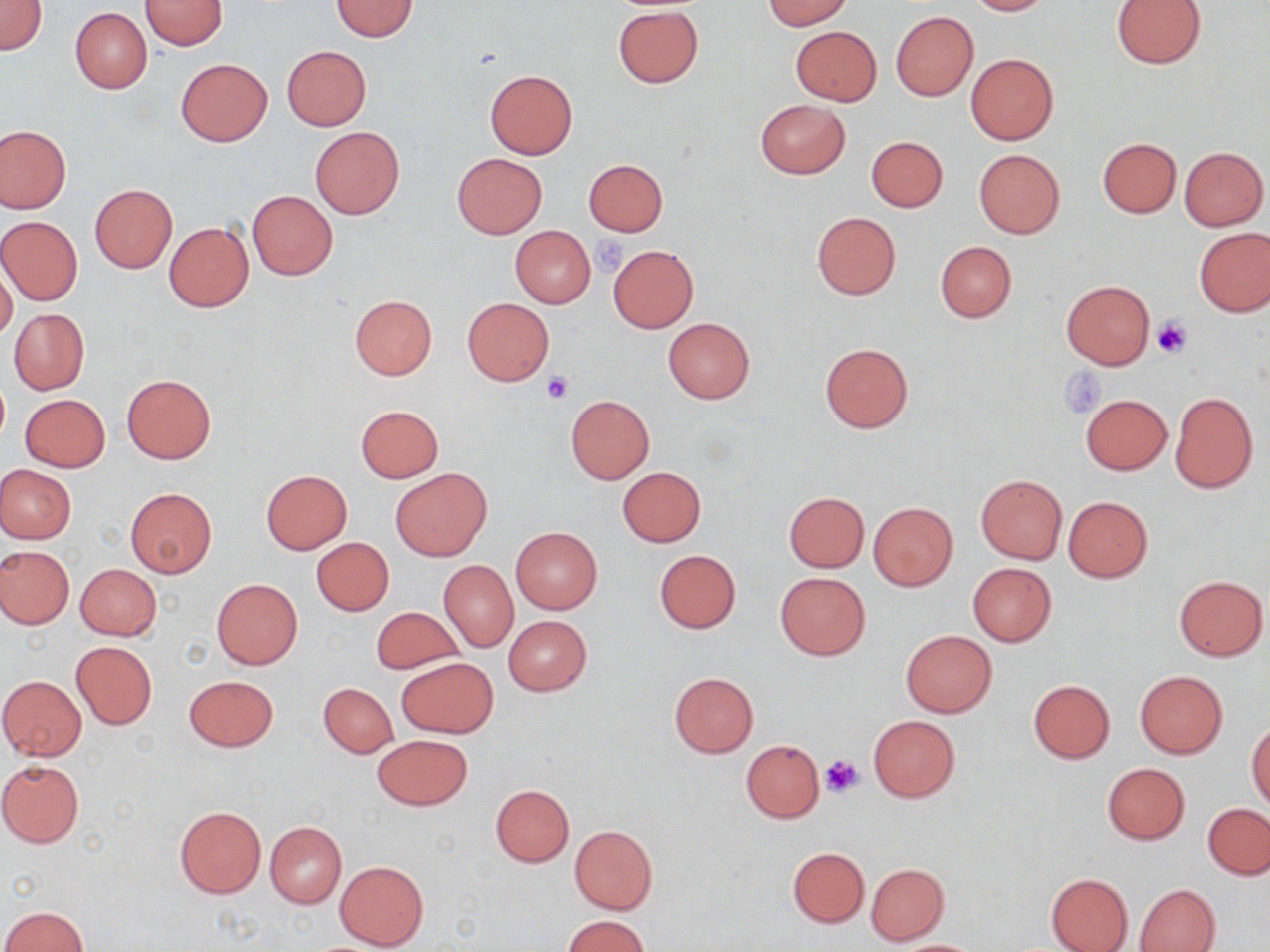

slide-level diagnosis = no evidence of blood parasites
magnification = 1000x
stain = May-Grünwald-Giemsa
modality = optical microscopy
platelet locations = approximate bounding boxes as (x1,y1)-(x2,y2) corner pairs in pixels: (584,228)-(626,276), (1151,319)-(1192,358), (1060,367)-(1106,418), (541,372)-(574,403), (821,753)-(865,796)
preparation = thin blood smear
field of view = one of a larger specimen
image size = 1270×952 pixels
uninfected red blood cell locations = approximate bounding boxes as (x1,y1)-(x2,y2) corner pairs in pixels: (0,0)-(46,56), (140,0)-(227,50), (332,0)-(418,41), (762,0)-(853,30), (965,0)-(1054,15), (1111,0)-(1207,69), (612,5)-(704,88), (70,7)-(151,93), (890,12)-(977,101), (791,26)-(881,104), (282,45)-(370,130), (966,54)-(1058,144), (176,58)-(272,145), (484,69)-(578,159), (756,98)-(850,179), (0,125)-(71,214), (309,127)-(405,219), (866,135)-(949,212), (1098,138)-(1180,218), (1179,147)-(1268,231), (974,149)-(1064,239), (452,153)-(547,238), (583,159)-(668,236), (89,184)-(177,272), (247,191)-(338,280), (812,211)-(901,299), (0,216)-(83,304), (164,222)-(253,312), (510,225)-(596,308), (1194,228)-(1269,317), (935,241)-(1016,322), (608,245)-(698,332), (0,263)-(17,342), (1060,280)-(1155,369), (350,295)-(437,380), (462,297)-(554,387), (9,309)-(89,394), (663,317)-(755,404), (820,342)-(914,432), (122,373)-(216,463), (0,378)-(9,446), (1169,391)-(1257,493), (21,394)-(110,472), (1080,394)-(1172,475), (566,396)-(654,483), (356,405)-(443,482), (0,465)-(75,543), (390,466)-(492,562), (616,466)-(707,547), (261,470)-(352,553), (975,474)-(1067,564), (125,488)-(216,578), (783,492)-(870,572), (1062,496)-(1153,582), (868,501)-(958,591), (511,527)-(602,614), (311,538)-(394,616), (0,546)-(75,629), (655,550)-(741,633), (440,561)-(518,651), (967,563)-(1057,647), (75,564)-(162,640), (775,571)-(870,660), (1174,575)-(1268,661), (212,579)-(302,670), (371,606)-(463,675), (504,615)-(592,696), (901,630)-(997,717), (71,640)-(156,730), (397,657)-(498,738), (1133,670)-(1228,759), (669,672)-(758,757), (0,675)-(87,760), (184,675)-(279,751), (1027,679)-(1115,763), (319,682)-(399,757), (867,715)-(960,802), (1247,723)-(1270,811), (372,734)-(472,811), (740,739)-(823,823), (1,759)-(85,847), (1102,762)-(1189,844), (490,785)-(574,866), (1203,803)-(1270,879), (174,806)-(267,898), (265,821)-(346,909), (569,825)-(658,914), (788,847)-(869,927), (335,860)-(428,949), (866,863)-(949,944), (1045,872)-(1134,952), (1135,884)-(1219,952), (2,905)-(87,952), (563,915)-(649,952), (890,940)-(984,952)